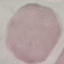 Result: no malaria parasites seen. Thin smear of blood. Giemsa stain. Photographed with a smartphone camera at the microscope eyepiece. Cell patch, automatically extracted from a larger field of view and resized to 64 × 64 pixels.